Classify this cell by malaria status.
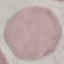

It is uninfected.

preparation = thin smear
capture = smartphone through the microscope eyepiece
image type = automatically extracted cell patch, resized to 64 × 64 pixels
stain = Giemsa